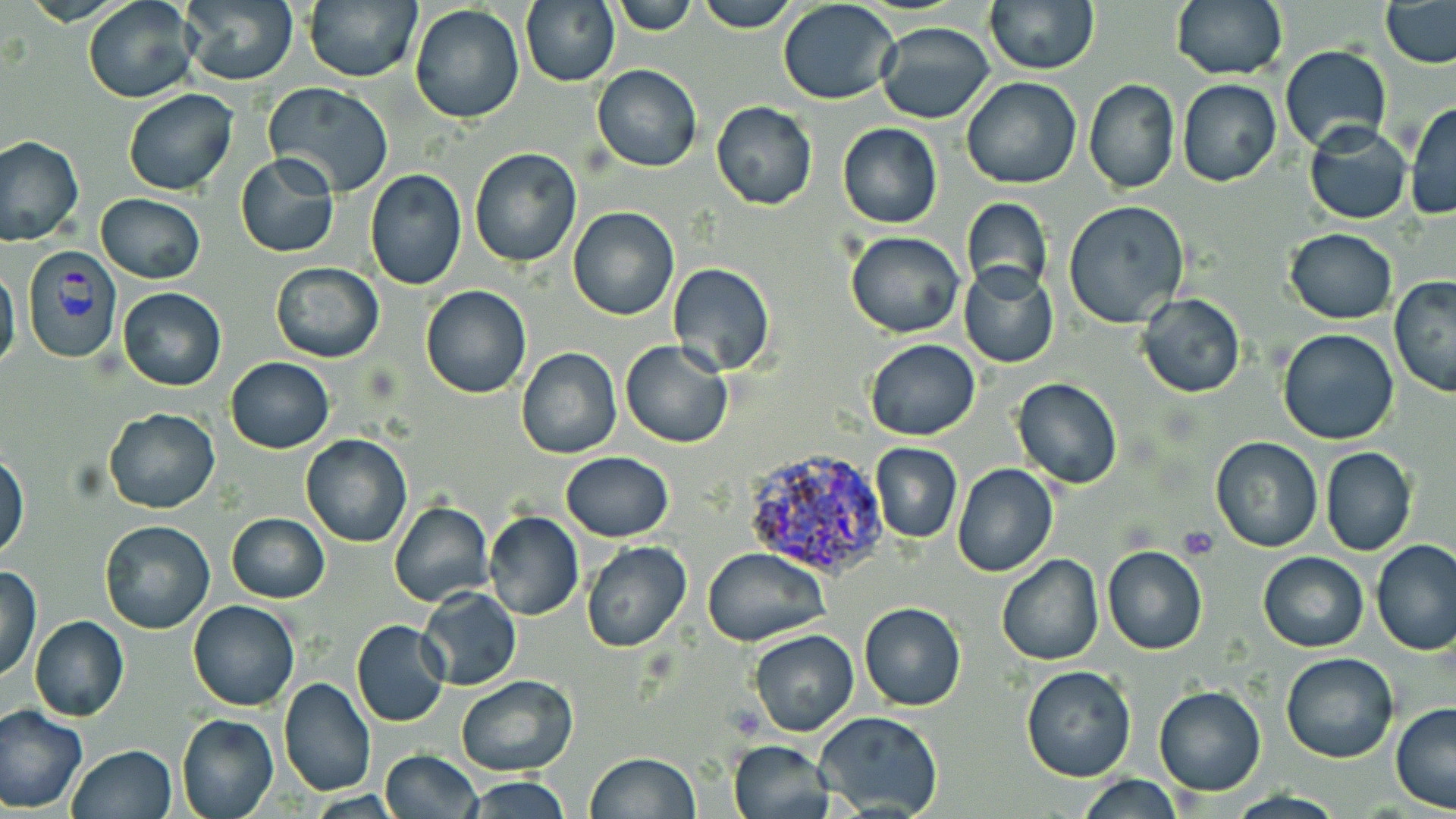
Summary:
  - Coordinate format: approximate bounding boxes as named x1/y1/x2/y2 corners in pixels
  - Plasmodium vivax-infected red blood cell locations: (x1=21, y1=247, x2=123, y2=364), (x1=740, y1=443, x2=891, y2=576)
  - Platelet locations: (x1=1179, y1=527, x2=1218, y2=558)
  - Uninfected red blood cell locations: (x1=83, y1=0, x2=200, y2=104), (x1=302, y1=0, x2=421, y2=83), (x1=611, y1=0, x2=699, y2=34), (x1=693, y1=0, x2=800, y2=32), (x1=984, y1=0, x2=1100, y2=75), (x1=1172, y1=0, x2=1287, y2=80), (x1=519, y1=1, x2=619, y2=87), (x1=777, y1=1, x2=903, y2=104), (x1=1379, y1=1, x2=1456, y2=68), (x1=180, y1=2, x2=299, y2=85), (x1=409, y1=5, x2=526, y2=124), (x1=875, y1=21, x2=994, y2=124), (x1=1279, y1=45, x2=1391, y2=151), (x1=591, y1=64, x2=703, y2=173), (x1=961, y1=77, x2=1083, y2=188), (x1=1084, y1=79, x2=1181, y2=195), (x1=1177, y1=79, x2=1282, y2=187), (x1=264, y1=82, x2=393, y2=197), (x1=122, y1=88, x2=237, y2=195), (x1=1406, y1=100, x2=1455, y2=220), (x1=711, y1=101, x2=819, y2=210), (x1=1303, y1=121, x2=1413, y2=225), (x1=838, y1=123, x2=943, y2=229), (x1=0, y1=136, x2=83, y2=247), (x1=469, y1=147, x2=583, y2=269), (x1=235, y1=152, x2=339, y2=259), (x1=367, y1=164, x2=579, y2=280), (x1=365, y1=169, x2=467, y2=291), (x1=96, y1=193, x2=205, y2=283), (x1=959, y1=197, x2=1053, y2=297), (x1=1063, y1=201, x2=1189, y2=328), (x1=568, y1=206, x2=680, y2=320), (x1=1285, y1=228, x2=1398, y2=323), (x1=845, y1=232, x2=966, y2=339), (x1=956, y1=262, x2=1060, y2=369), (x1=269, y1=263, x2=384, y2=362), (x1=666, y1=263, x2=776, y2=376), (x1=0, y1=265, x2=21, y2=376), (x1=1389, y1=275, x2=1456, y2=397), (x1=421, y1=284, x2=532, y2=398), (x1=118, y1=287, x2=227, y2=391), (x1=1136, y1=292, x2=1247, y2=398), (x1=1278, y1=327, x2=1400, y2=445), (x1=620, y1=339, x2=734, y2=450), (x1=864, y1=339, x2=980, y2=440), (x1=516, y1=347, x2=622, y2=460), (x1=224, y1=356, x2=334, y2=453), (x1=1011, y1=378, x2=1123, y2=488), (x1=102, y1=407, x2=219, y2=513), (x1=301, y1=433, x2=413, y2=548), (x1=1210, y1=435, x2=1323, y2=551), (x1=870, y1=441, x2=963, y2=543), (x1=1320, y1=446, x2=1417, y2=558), (x1=0, y1=452, x2=29, y2=560), (x1=559, y1=452, x2=674, y2=541), (x1=952, y1=463, x2=1059, y2=579), (x1=389, y1=500, x2=493, y2=606), (x1=483, y1=511, x2=584, y2=622), (x1=227, y1=512, x2=330, y2=603), (x1=100, y1=521, x2=215, y2=633), (x1=1371, y1=539, x2=1456, y2=656), (x1=582, y1=540, x2=692, y2=652), (x1=1101, y1=544, x2=1208, y2=655), (x1=703, y1=546, x2=832, y2=647), (x1=1258, y1=551, x2=1368, y2=652), (x1=996, y1=555, x2=1104, y2=666), (x1=1, y1=565, x2=41, y2=681), (x1=418, y1=587, x2=521, y2=692), (x1=187, y1=599, x2=299, y2=712), (x1=859, y1=602, x2=967, y2=711), (x1=28, y1=615, x2=128, y2=723), (x1=350, y1=618, x2=451, y2=727), (x1=748, y1=629, x2=859, y2=736), (x1=1280, y1=650, x2=1399, y2=763), (x1=1021, y1=665, x2=1137, y2=782), (x1=277, y1=675, x2=377, y2=799), (x1=456, y1=675, x2=578, y2=776), (x1=1154, y1=686, x2=1266, y2=796), (x1=1390, y1=704, x2=1456, y2=813), (x1=0, y1=705, x2=89, y2=814), (x1=815, y1=710, x2=945, y2=818), (x1=176, y1=711, x2=278, y2=819), (x1=730, y1=738, x2=837, y2=819), (x1=68, y1=744, x2=177, y2=819), (x1=380, y1=750, x2=481, y2=818), (x1=586, y1=752, x2=702, y2=819), (x1=1076, y1=775, x2=1184, y2=817), (x1=465, y1=776, x2=574, y2=818)
  - Slide-level diagnosis: Plasmodium vivax
  - Preparation: thin blood film
  - Modality: light microscopy
  - Magnification: 1000x
  - Stain: May-Grünwald-Giemsa
  - Field of view: one of a larger specimen
  - Image size: 1456×819 pixels